Assess the morphology of the erythrocytes.
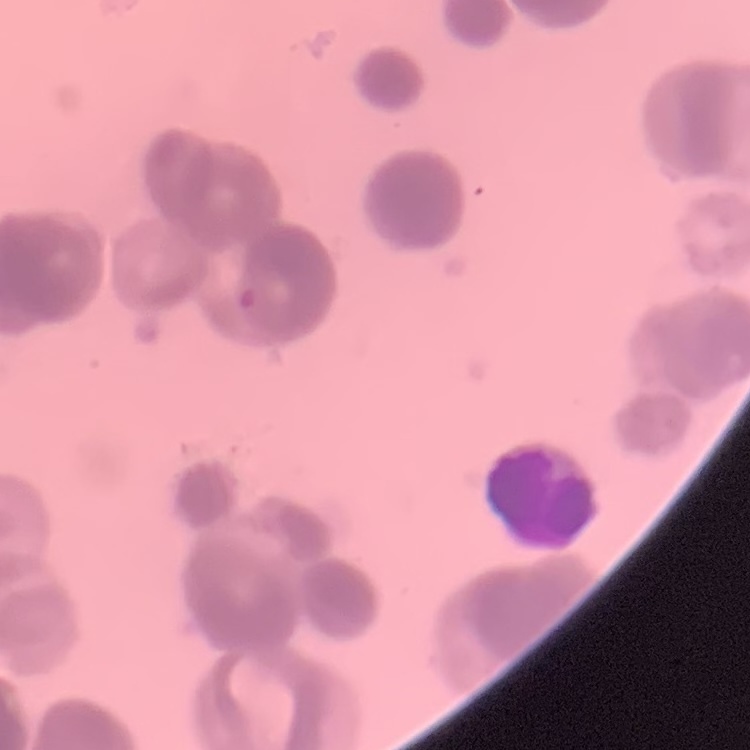

Rouleaux formation.

One tile cut from a larger photomicrograph. Thin blood smear. Stained with either Field's or Giemsa.